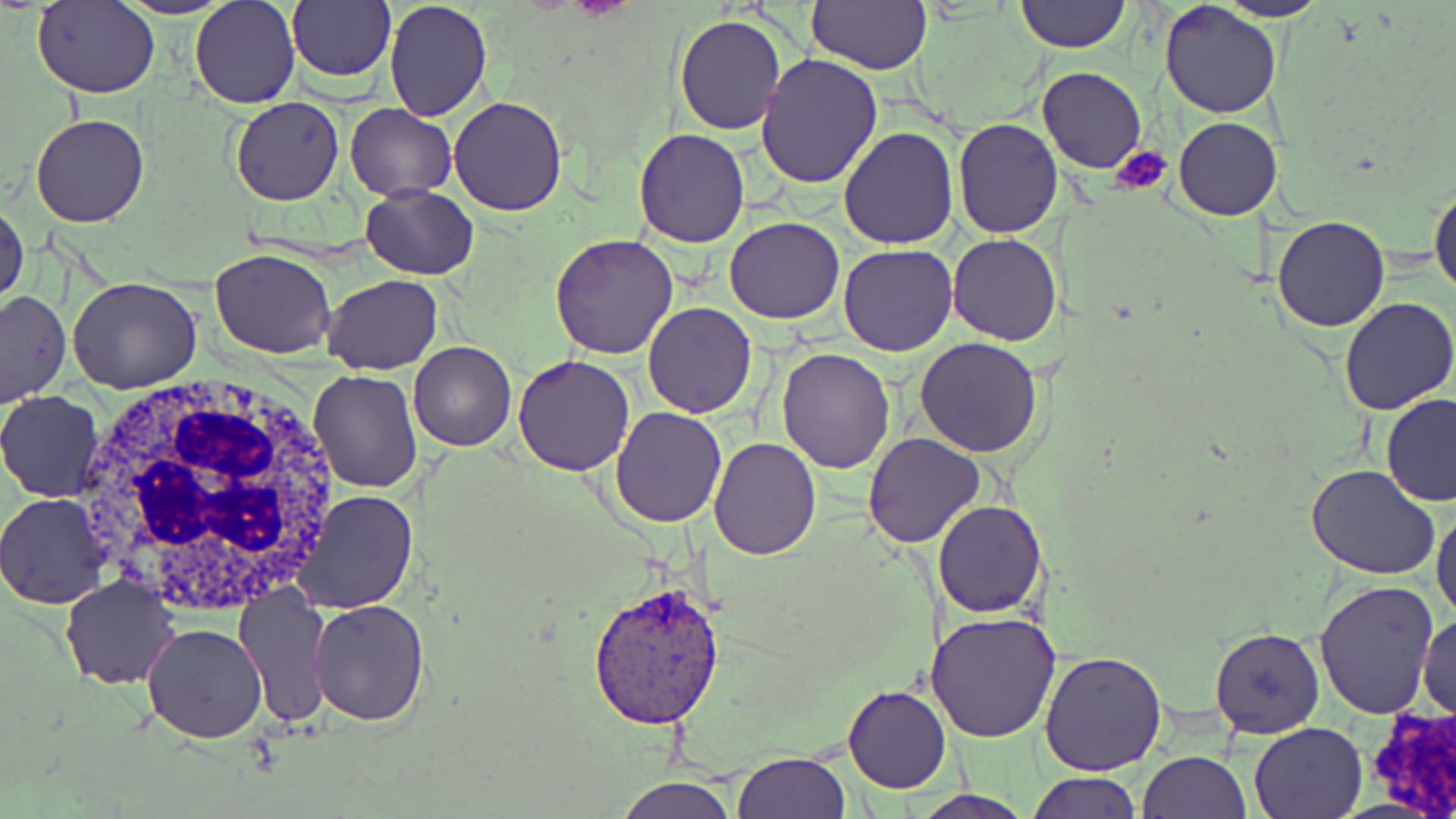
Summary:
  - Coordinate format: approximate bounding boxes as named x1/y1/x2/y2 corners in pixels
  - Plasmodium vivax-infected red blood cell locations: (x1=589, y1=581, x2=725, y2=728)
  - White blood cell locations: (x1=72, y1=374, x2=349, y2=611)
  - Platelet locations: (x1=1109, y1=145, x2=1173, y2=196)
  - Uninfected red blood cell locations: (x1=32, y1=0, x2=160, y2=99), (x1=114, y1=0, x2=234, y2=19), (x1=190, y1=0, x2=299, y2=109), (x1=286, y1=0, x2=395, y2=83), (x1=384, y1=0, x2=493, y2=120), (x1=1013, y1=0, x2=1131, y2=52), (x1=1159, y1=0, x2=1284, y2=120), (x1=1217, y1=0, x2=1330, y2=22), (x1=804, y1=1, x2=931, y2=74), (x1=674, y1=14, x2=788, y2=135), (x1=755, y1=54, x2=885, y2=189), (x1=1037, y1=66, x2=1146, y2=175), (x1=230, y1=96, x2=345, y2=205), (x1=448, y1=96, x2=568, y2=217), (x1=345, y1=103, x2=457, y2=200), (x1=31, y1=112, x2=149, y2=228), (x1=1172, y1=116, x2=1279, y2=220), (x1=951, y1=118, x2=1064, y2=238), (x1=839, y1=125, x2=959, y2=248), (x1=635, y1=129, x2=750, y2=247), (x1=1430, y1=178, x2=1456, y2=301), (x1=360, y1=185, x2=478, y2=279), (x1=0, y1=198, x2=28, y2=308), (x1=1272, y1=215, x2=1391, y2=332), (x1=725, y1=217, x2=846, y2=323), (x1=948, y1=233, x2=1062, y2=346), (x1=548, y1=234, x2=678, y2=358), (x1=838, y1=244, x2=957, y2=355), (x1=211, y1=249, x2=337, y2=358), (x1=68, y1=275, x2=203, y2=392), (x1=321, y1=275, x2=443, y2=375), (x1=0, y1=291, x2=71, y2=407), (x1=1337, y1=298, x2=1456, y2=416), (x1=643, y1=304, x2=755, y2=418), (x1=915, y1=337, x2=1043, y2=457), (x1=409, y1=342, x2=516, y2=451), (x1=777, y1=347, x2=894, y2=472), (x1=514, y1=355, x2=635, y2=476), (x1=309, y1=369, x2=422, y2=493), (x1=0, y1=390, x2=105, y2=502), (x1=1380, y1=395, x2=1456, y2=506), (x1=609, y1=407, x2=729, y2=527), (x1=863, y1=433, x2=984, y2=548), (x1=708, y1=437, x2=821, y2=559), (x1=1305, y1=464, x2=1440, y2=583), (x1=291, y1=488, x2=419, y2=613), (x1=0, y1=494, x2=111, y2=609), (x1=934, y1=502, x2=1046, y2=618), (x1=1432, y1=506, x2=1456, y2=627), (x1=60, y1=574, x2=181, y2=691), (x1=1313, y1=581, x2=1441, y2=721), (x1=233, y1=585, x2=333, y2=727), (x1=309, y1=598, x2=432, y2=725), (x1=927, y1=611, x2=1060, y2=742), (x1=1417, y1=614, x2=1455, y2=723), (x1=142, y1=623, x2=267, y2=743), (x1=1209, y1=626, x2=1326, y2=740), (x1=1040, y1=648, x2=1167, y2=776), (x1=842, y1=684, x2=950, y2=795), (x1=1247, y1=721, x2=1366, y2=819), (x1=1140, y1=748, x2=1250, y2=818), (x1=733, y1=749, x2=852, y2=818), (x1=1025, y1=771, x2=1143, y2=819), (x1=612, y1=776, x2=739, y2=819), (x1=908, y1=790, x2=1038, y2=819)
  - Slide-level diagnosis: Plasmodium vivax
  - Field of view: one of a larger specimen
  - Stain: May-Grünwald-Giemsa
  - Image size: 1456×819 pixels
  - Magnification: 1000x
  - Modality: light microscopy
  - Preparation: thin blood film